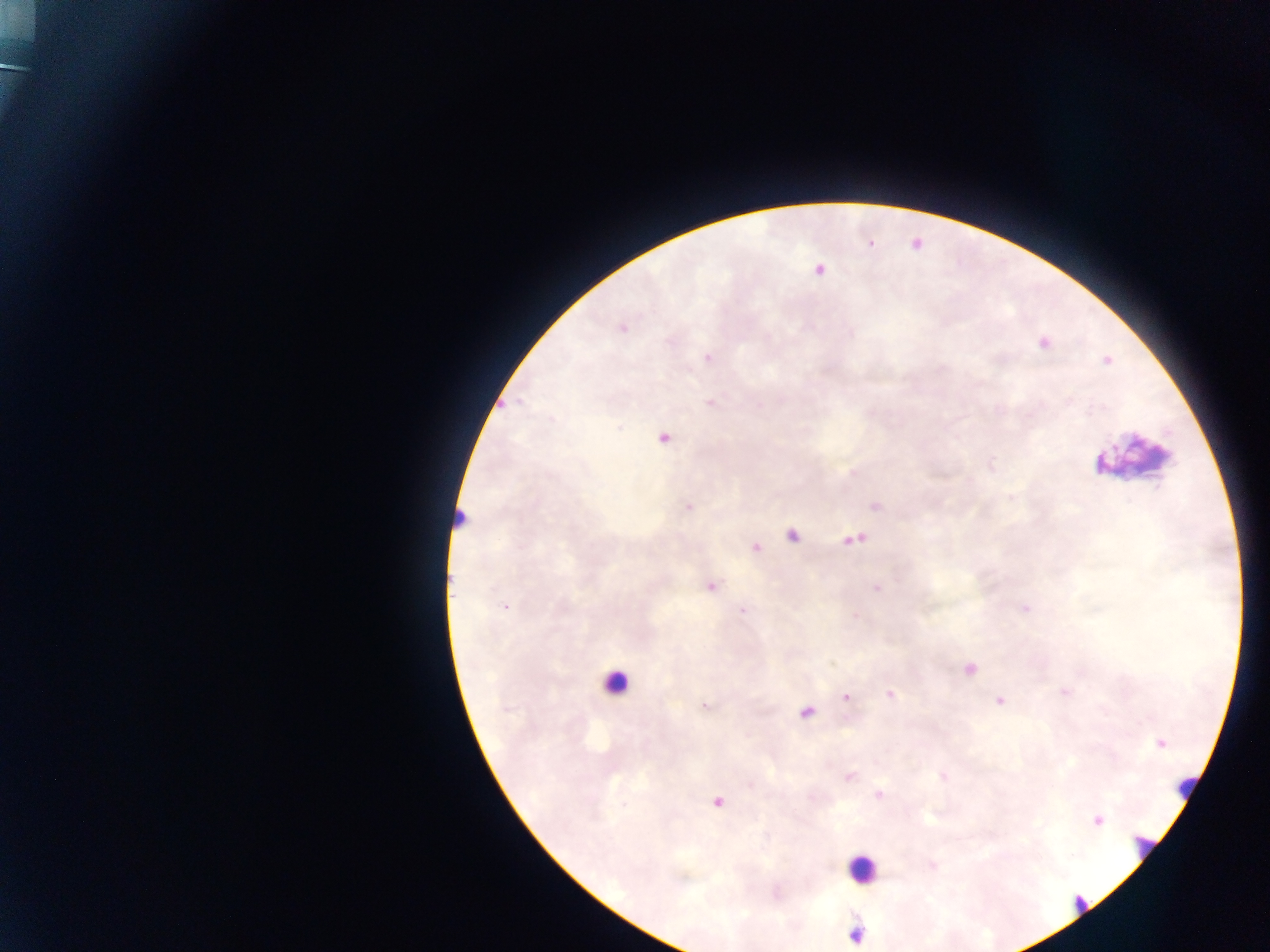

Approximate centers as x y in pixels. Malaria parasite locations: 871 242; 818 268; 622 328; 1042 344; 708 357; 510 405; 662 437; 688 507; 792 535; 754 547; 710 586; 877 587; 504 606; 743 610; 891 694; 845 697; 1001 701; 705 705; 807 711; 1160 744; 849 777; 878 794; 717 801; 1097 820. Leukocyte locations: 613 683; 860 873. Collected in Ghana. One field of view. Image is 1270×952 pixels. Thick blood film. Mobile-phone photograph taken through the microscope.